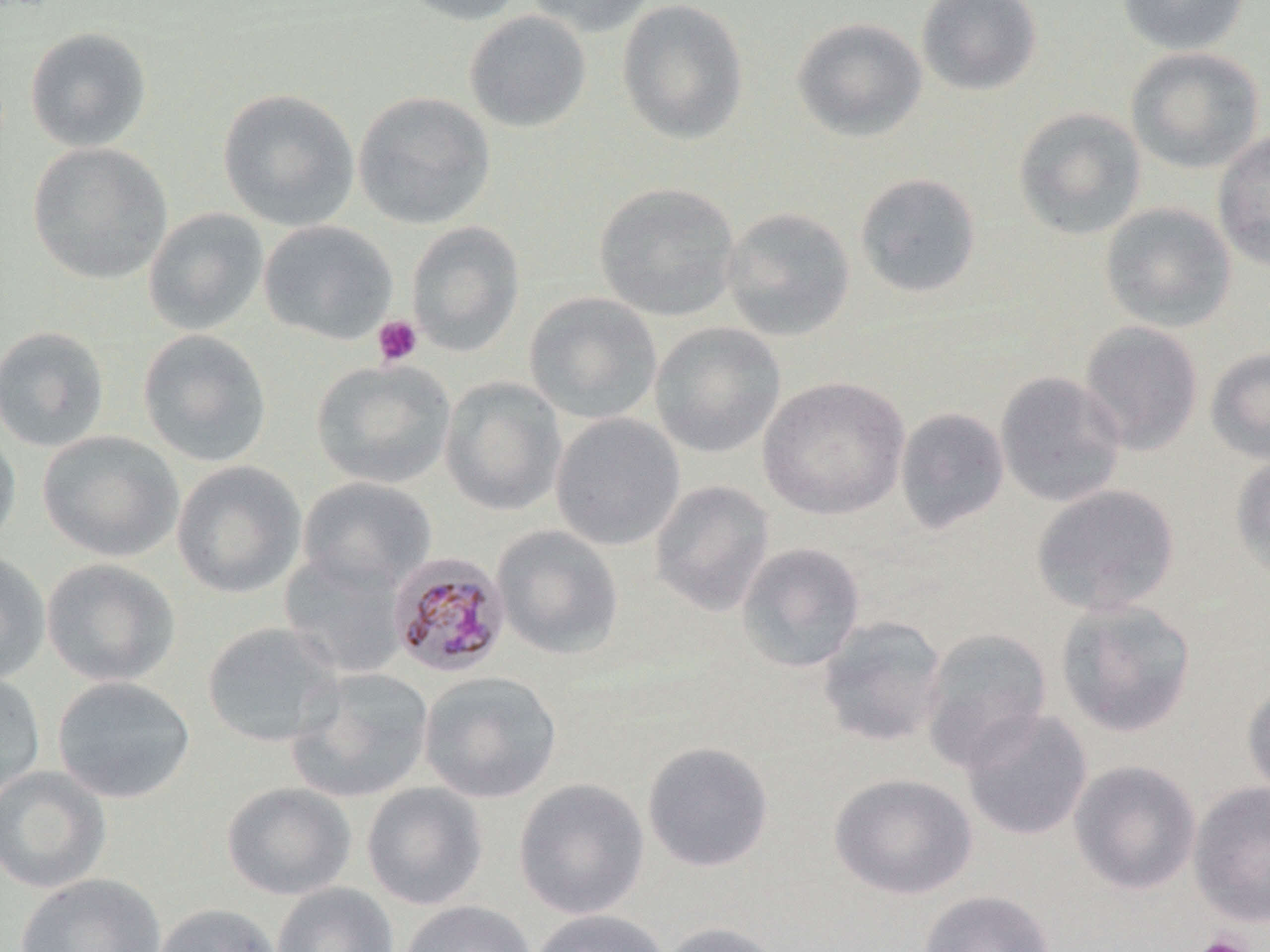
Approximate bounding boxes as (x1, y1, x2, y2) in pixels. Uninfected red blood cell locations: (397, 0, 527, 25), (524, 0, 659, 37), (916, 0, 1043, 96), (1117, 0, 1250, 56), (616, 1, 749, 144), (464, 11, 591, 133), (791, 17, 927, 142), (25, 27, 152, 152), (1125, 46, 1264, 175), (217, 88, 360, 231), (352, 91, 496, 230), (1013, 107, 1147, 240), (1212, 130, 1270, 271), (27, 142, 173, 285), (854, 172, 982, 299), (593, 181, 740, 321), (1099, 202, 1237, 332), (721, 206, 856, 342), (142, 207, 268, 336), (259, 220, 397, 344), (406, 221, 525, 356), (524, 292, 662, 424), (1078, 320, 1204, 455), (649, 321, 786, 459), (0, 326, 110, 452), (138, 329, 272, 468), (1206, 347, 1270, 465), (311, 358, 456, 489), (994, 371, 1127, 508), (758, 375, 910, 520), (440, 376, 567, 516), (894, 407, 1010, 535), (550, 413, 685, 551), (0, 422, 21, 554), (37, 430, 183, 562), (1230, 454, 1270, 579), (171, 460, 307, 599), (297, 477, 437, 593), (649, 479, 776, 616), (1031, 483, 1180, 616), (491, 525, 624, 660), (736, 542, 866, 673), (279, 549, 408, 679), (0, 551, 51, 684), (40, 558, 180, 687), (1056, 599, 1197, 738), (816, 615, 948, 747), (201, 621, 344, 748), (920, 627, 1052, 771), (287, 667, 434, 804), (418, 671, 562, 804), (0, 672, 46, 800), (52, 675, 196, 804), (1241, 676, 1270, 803), (959, 707, 1093, 841), (642, 741, 774, 872), (1068, 759, 1201, 895), (0, 765, 111, 894), (828, 773, 978, 900), (513, 778, 650, 920), (221, 781, 357, 900), (361, 781, 489, 910), (1188, 781, 1270, 927), (15, 873, 166, 952), (271, 882, 398, 952), (919, 889, 1055, 952), (399, 900, 537, 952), (153, 902, 282, 952), (526, 909, 672, 952), (656, 921, 785, 952). Plasmodium malariae-infected red blood cell locations: (387, 553, 511, 679). Platelet locations: (372, 315, 423, 367), (1190, 934, 1255, 952). Slide-level diagnosis: Plasmodium malariae. Captured at 1000x magnification. Thin blood smear. Light microscopy. May-Grünwald-Giemsa stain. Image is 1270×952 pixels. Single field of view.